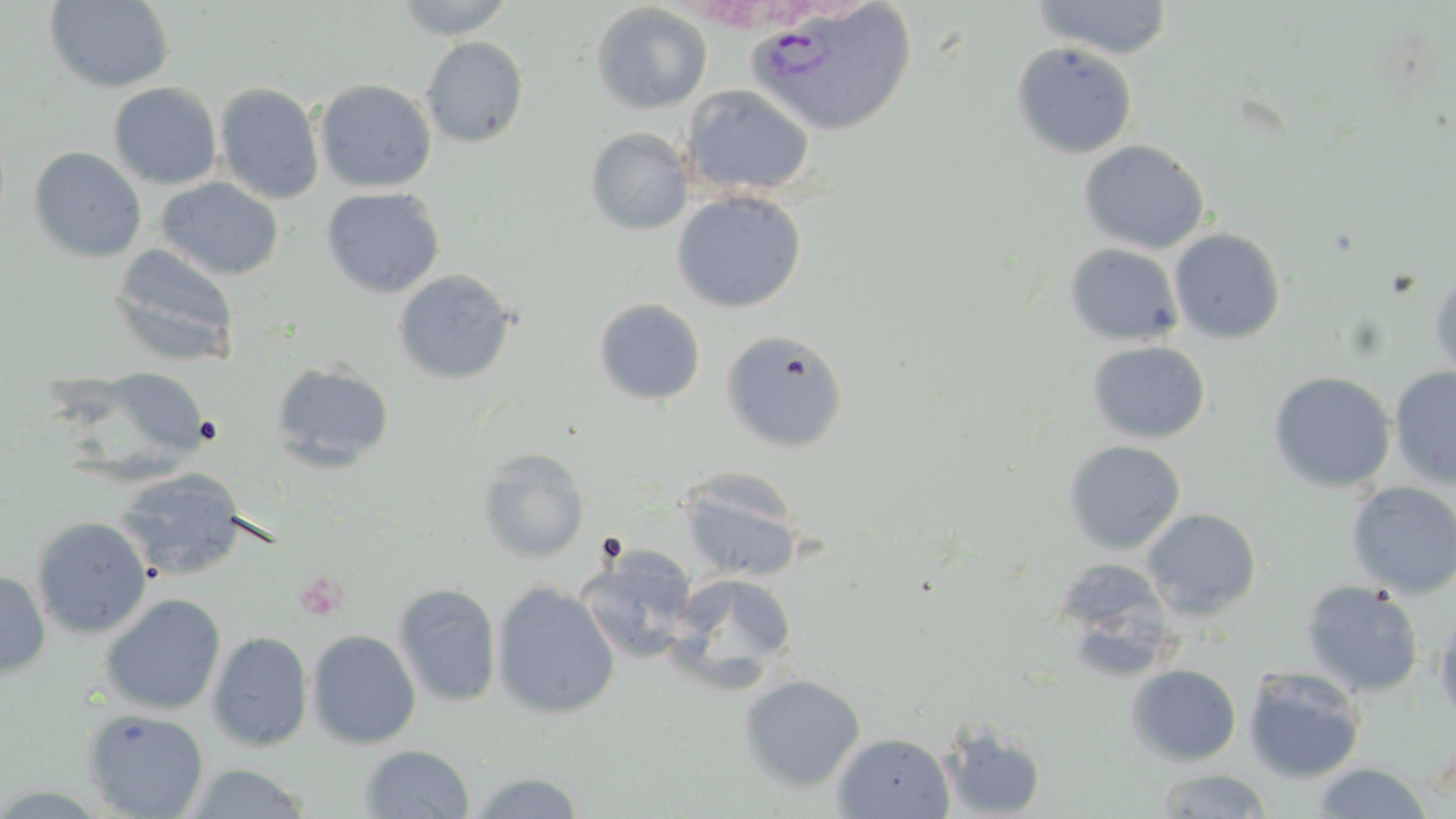
Approximate bounding boxes as named x1/y1/x2/y2 corners in pixels. Plasmodium vivax-infected red blood cell locations: (x1=745, y1=0, x2=916, y2=138). Uninfected red blood cell locations: (x1=392, y1=0, x2=515, y2=39), (x1=43, y1=1, x2=175, y2=93), (x1=1030, y1=1, x2=1175, y2=60), (x1=590, y1=3, x2=713, y2=115), (x1=421, y1=36, x2=529, y2=148), (x1=1010, y1=41, x2=1138, y2=159), (x1=314, y1=78, x2=437, y2=193), (x1=108, y1=82, x2=222, y2=189), (x1=215, y1=82, x2=325, y2=205), (x1=680, y1=85, x2=815, y2=197), (x1=585, y1=127, x2=693, y2=235), (x1=1078, y1=140, x2=1210, y2=254), (x1=28, y1=146, x2=147, y2=263), (x1=157, y1=177, x2=284, y2=280), (x1=321, y1=186, x2=445, y2=298), (x1=671, y1=190, x2=807, y2=313), (x1=1169, y1=228, x2=1287, y2=344), (x1=110, y1=244, x2=239, y2=367), (x1=1064, y1=244, x2=1183, y2=346), (x1=1429, y1=268, x2=1456, y2=382), (x1=393, y1=269, x2=517, y2=384), (x1=593, y1=298, x2=706, y2=405), (x1=720, y1=329, x2=850, y2=453), (x1=1087, y1=340, x2=1210, y2=444), (x1=271, y1=361, x2=395, y2=471), (x1=1389, y1=366, x2=1456, y2=488), (x1=1267, y1=371, x2=1396, y2=492), (x1=1062, y1=440, x2=1187, y2=555), (x1=477, y1=447, x2=590, y2=562), (x1=115, y1=469, x2=246, y2=581), (x1=677, y1=470, x2=807, y2=583), (x1=1347, y1=481, x2=1456, y2=599), (x1=1140, y1=508, x2=1262, y2=620), (x1=30, y1=515, x2=153, y2=638), (x1=577, y1=546, x2=700, y2=663), (x1=0, y1=569, x2=50, y2=678), (x1=668, y1=572, x2=799, y2=687), (x1=491, y1=580, x2=621, y2=720), (x1=1301, y1=580, x2=1424, y2=698), (x1=392, y1=582, x2=502, y2=708), (x1=101, y1=592, x2=226, y2=715), (x1=1433, y1=609, x2=1456, y2=728), (x1=306, y1=629, x2=421, y2=748), (x1=207, y1=630, x2=314, y2=752), (x1=1125, y1=663, x2=1242, y2=767), (x1=1242, y1=666, x2=1367, y2=783), (x1=738, y1=674, x2=866, y2=793), (x1=83, y1=708, x2=209, y2=819), (x1=941, y1=722, x2=1047, y2=818), (x1=832, y1=732, x2=955, y2=818), (x1=360, y1=744, x2=475, y2=818), (x1=1311, y1=761, x2=1434, y2=818), (x1=181, y1=762, x2=314, y2=818), (x1=1154, y1=767, x2=1275, y2=818), (x1=465, y1=770, x2=589, y2=818). Platelet locations: (x1=295, y1=569, x2=350, y2=619). Slide-level diagnosis: Plasmodium vivax. Image is 1456×819 pixels. Single field of view. 1000x magnification. Light microscopy. Thin blood film. May-Grünwald-Giemsa stain.